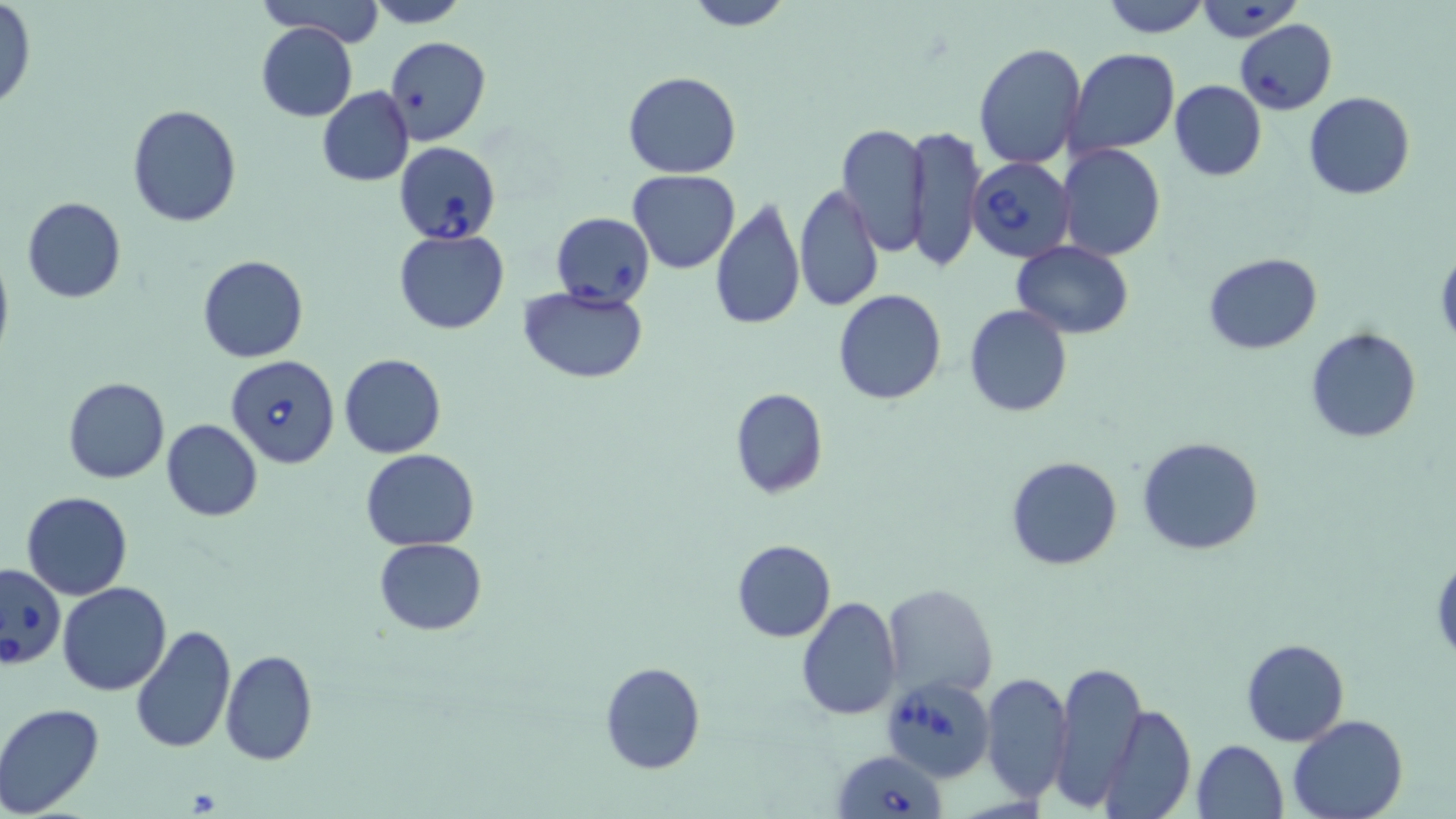

Approximate bounding boxes as [x1, y1, x2, y2] in pixels. Uninfected red blood cell locations: [253, 0, 384, 46], [363, 0, 473, 27], [679, 0, 795, 31], [1100, 0, 1211, 37], [1194, 1, 1306, 43], [0, 2, 36, 111], [255, 21, 358, 122], [386, 36, 491, 146], [972, 44, 1087, 169], [1066, 49, 1181, 159], [623, 71, 741, 178], [1169, 80, 1267, 181], [317, 87, 414, 187], [1305, 91, 1415, 200], [128, 102, 242, 227], [836, 123, 930, 259], [904, 124, 984, 270], [1056, 144, 1167, 262], [628, 169, 740, 273], [793, 183, 884, 313], [709, 195, 804, 334], [22, 197, 126, 304], [394, 229, 510, 334], [1011, 240, 1133, 339], [0, 246, 13, 368], [1436, 248, 1456, 349], [1205, 252, 1322, 353], [198, 255, 307, 364], [520, 287, 648, 384], [833, 289, 947, 405], [965, 304, 1072, 417], [1305, 327, 1422, 443], [339, 353, 446, 458], [63, 377, 169, 483], [729, 389, 828, 498], [161, 419, 263, 522], [1136, 436, 1264, 556], [360, 449, 479, 551], [1006, 455, 1123, 569], [23, 491, 133, 599], [373, 539, 487, 635], [731, 540, 836, 642], [1431, 552, 1455, 660], [57, 582, 171, 696], [880, 582, 998, 699], [796, 596, 901, 720], [131, 623, 237, 756], [1240, 638, 1350, 747], [220, 648, 317, 764], [1052, 660, 1145, 809], [600, 661, 704, 773], [981, 673, 1073, 805], [1099, 703, 1195, 818], [0, 704, 108, 819], [1287, 715, 1408, 819], [1193, 738, 1289, 819]. Babesia divergens-infected red blood cell locations: [1234, 20, 1337, 114], [395, 142, 501, 243], [966, 158, 1075, 263], [551, 212, 655, 309], [225, 354, 342, 468], [0, 561, 66, 670], [887, 677, 998, 789], [833, 748, 945, 819]. Slide-level diagnosis: Babesia divergens. Single field of view. 1000x magnification. Thin blood smear. Light microscopy. Image is 1456×819 pixels. May-Grünwald-Giemsa stain.